Give the position of every Plasmodium parasite visible.
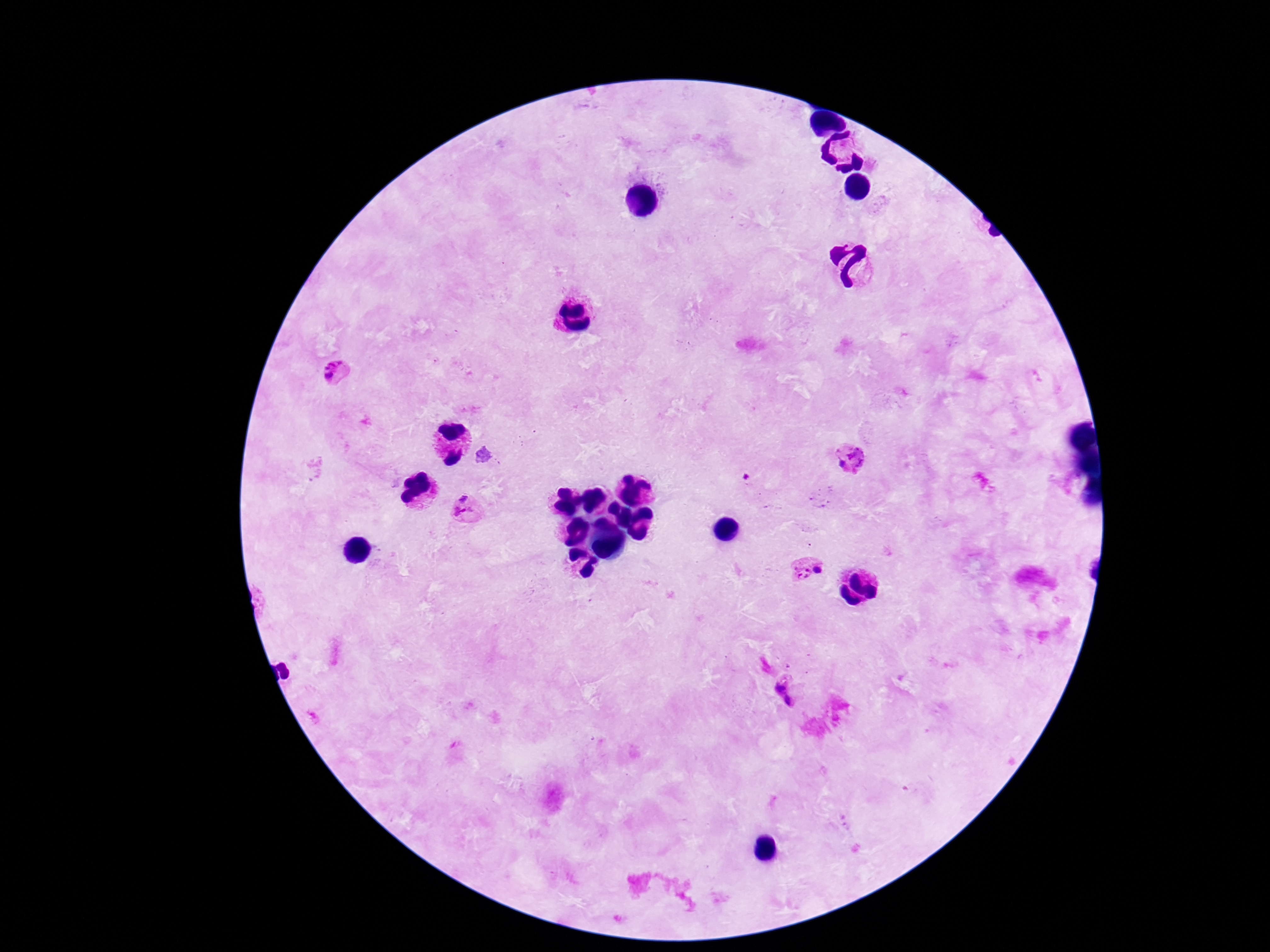
Approximate centers as [x, y] in pixels.
Plasmodium parasites: [333, 361], [329, 377], [859, 455], [840, 463], [462, 496], [463, 516], [819, 570], [800, 574], [780, 687], [789, 701].

Summary:
  - Capture: smartphone camera through the microscope eyepiece
  - Image size: 1270×952 pixels
  - Magnification: 100x
  - Preparation: thick peripheral-blood smear
  - Field of view: single
  - Stain: Giemsa
  - Patient malaria status: positive